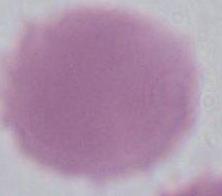

Summary:
  - Identification: red blood cell
  - Modality: micrograph
  - Magnification: 1000x